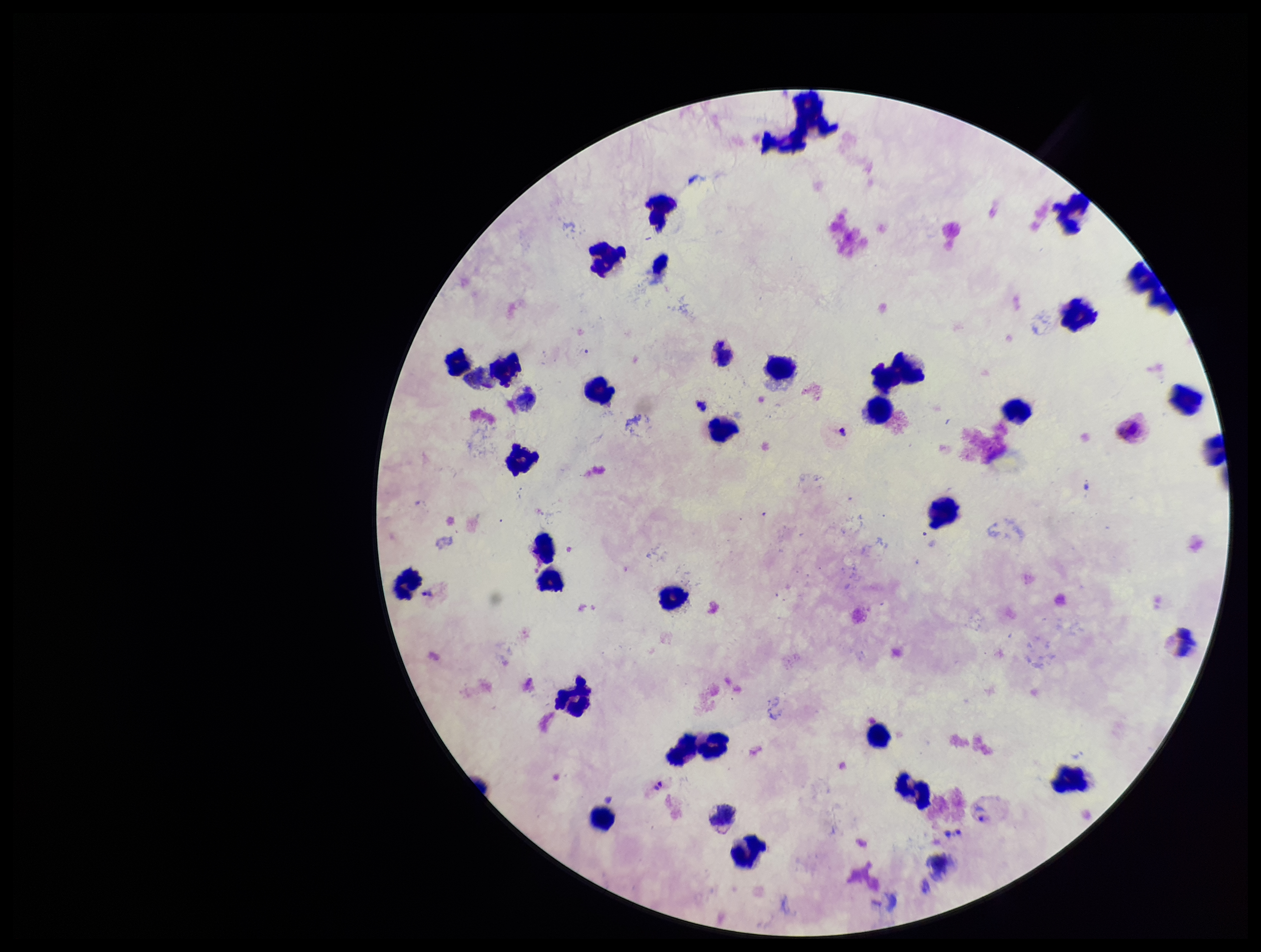 One field from this slide. Parasite count: 2. Image is 1261×952 pixels. Giemsa stain. Patient malaria status: positive. Species reported for this patient: Plasmodium vivax. Photographed through the microscope eyepiece with a smartphone camera. Leukocyte count: 30. Preparation: thick blood smear. Plasmodium parasites: seen.